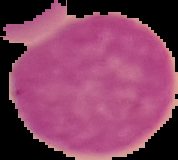

image size = 178×160 pixels
preparation = thin blood film
result = negative for Plasmodium parasites
image type = cell region segmented out of the field of view; surrounding area masked to black